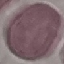

Summary:
  - Malaria status: uninfected
  - Stain: Giemsa
  - Capture: smartphone camera at the microscope eyepiece
  - Preparation: thin blood film
  - Image type: cell patch, automatically extracted from a larger field of view and resized to 64 × 64 pixels